State which parasite is depicted.
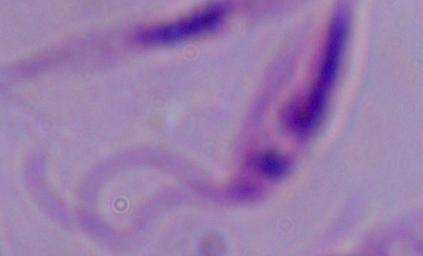

Leishmania.

modality = photomicrograph
magnification = 1000x